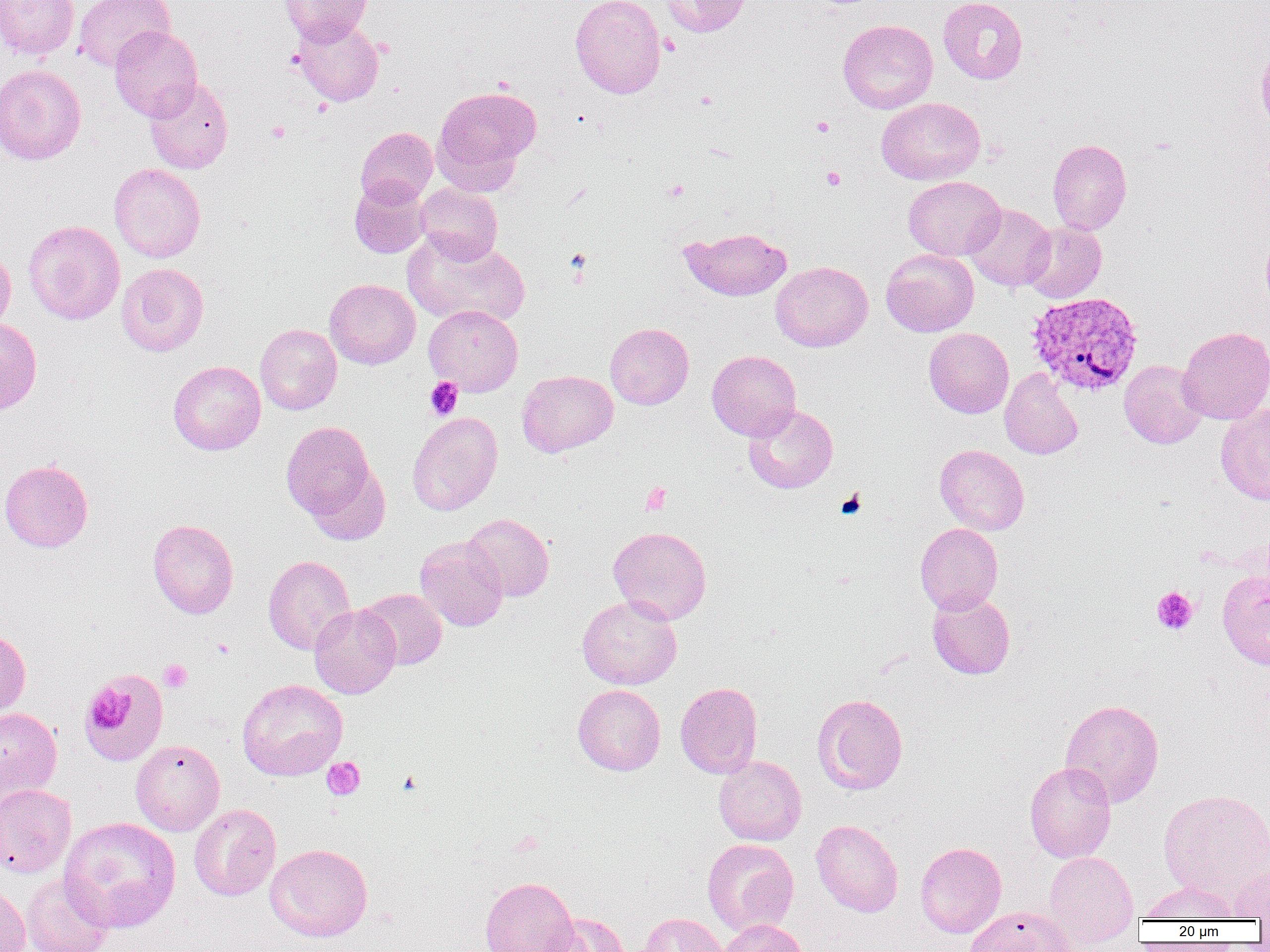
Approximate bounding boxes as named x1/y1/x2/y2 corners in pixels. Platelet locations (subset): (x1=811, y1=116, x2=834, y2=137), (x1=266, y1=121, x2=290, y2=143), (x1=821, y1=166, x2=846, y2=190), (x1=664, y1=179, x2=689, y2=201), (x1=425, y1=378, x2=463, y2=420), (x1=641, y1=482, x2=671, y2=515), (x1=836, y1=490, x2=866, y2=519), (x1=1151, y1=586, x2=1198, y2=634), (x1=158, y1=659, x2=192, y2=693), (x1=83, y1=686, x2=130, y2=733), (x1=322, y1=757, x2=365, y2=800), (x1=397, y1=771, x2=423, y2=796). Plasmodium vivax-infected red blood cell locations: (x1=1026, y1=291, x2=1144, y2=396). Uninfected red blood cell locations (subset): (x1=0, y1=0, x2=79, y2=61), (x1=73, y1=0, x2=174, y2=72), (x1=279, y1=0, x2=371, y2=45), (x1=570, y1=0, x2=666, y2=98), (x1=659, y1=0, x2=751, y2=37), (x1=939, y1=0, x2=1028, y2=84), (x1=291, y1=16, x2=384, y2=107), (x1=837, y1=19, x2=938, y2=114), (x1=109, y1=25, x2=202, y2=121), (x1=1256, y1=45, x2=1270, y2=134), (x1=0, y1=64, x2=87, y2=165), (x1=144, y1=78, x2=234, y2=174), (x1=433, y1=85, x2=540, y2=185), (x1=877, y1=97, x2=985, y2=185), (x1=355, y1=126, x2=438, y2=207), (x1=1047, y1=139, x2=1132, y2=235), (x1=109, y1=163, x2=206, y2=263), (x1=903, y1=176, x2=1005, y2=260), (x1=350, y1=179, x2=432, y2=258), (x1=416, y1=183, x2=503, y2=264), (x1=965, y1=204, x2=1055, y2=292), (x1=24, y1=220, x2=125, y2=325), (x1=1022, y1=222, x2=1107, y2=303), (x1=679, y1=227, x2=792, y2=301), (x1=1260, y1=229, x2=1270, y2=308), (x1=402, y1=232, x2=531, y2=329), (x1=0, y1=247, x2=15, y2=333), (x1=881, y1=248, x2=979, y2=337), (x1=770, y1=261, x2=873, y2=351), (x1=116, y1=262, x2=209, y2=356), (x1=324, y1=279, x2=420, y2=369), (x1=424, y1=305, x2=523, y2=396), (x1=0, y1=317, x2=42, y2=413), (x1=255, y1=323, x2=342, y2=415), (x1=605, y1=323, x2=694, y2=409), (x1=1177, y1=326, x2=1270, y2=424), (x1=924, y1=327, x2=1013, y2=418), (x1=707, y1=350, x2=801, y2=440), (x1=168, y1=360, x2=266, y2=455), (x1=1119, y1=360, x2=1207, y2=448), (x1=1000, y1=368, x2=1083, y2=459), (x1=517, y1=370, x2=618, y2=457), (x1=1216, y1=403, x2=1270, y2=505), (x1=743, y1=404, x2=838, y2=493), (x1=407, y1=412, x2=502, y2=515), (x1=281, y1=421, x2=378, y2=523), (x1=934, y1=444, x2=1029, y2=535), (x1=929, y1=445, x2=1012, y2=614), (x1=0, y1=459, x2=93, y2=552), (x1=306, y1=462, x2=390, y2=546), (x1=462, y1=513, x2=554, y2=601), (x1=147, y1=519, x2=239, y2=618), (x1=915, y1=523, x2=1003, y2=614), (x1=608, y1=525, x2=712, y2=624), (x1=414, y1=535, x2=509, y2=631), (x1=263, y1=555, x2=356, y2=655), (x1=1218, y1=570, x2=1270, y2=668), (x1=358, y1=588, x2=447, y2=669), (x1=927, y1=591, x2=1015, y2=679), (x1=577, y1=595, x2=682, y2=690), (x1=309, y1=604, x2=401, y2=699), (x1=0, y1=627, x2=30, y2=720), (x1=237, y1=678, x2=347, y2=780), (x1=675, y1=682, x2=762, y2=778), (x1=573, y1=684, x2=666, y2=775), (x1=812, y1=694, x2=908, y2=795), (x1=1060, y1=698, x2=1164, y2=808), (x1=0, y1=707, x2=62, y2=805), (x1=131, y1=740, x2=225, y2=835), (x1=713, y1=756, x2=806, y2=845), (x1=1024, y1=761, x2=1116, y2=863), (x1=0, y1=784, x2=76, y2=878), (x1=1158, y1=788, x2=1270, y2=906), (x1=189, y1=804, x2=281, y2=901), (x1=59, y1=816, x2=181, y2=933), (x1=811, y1=819, x2=903, y2=917), (x1=701, y1=838, x2=799, y2=936), (x1=915, y1=842, x2=1007, y2=937), (x1=265, y1=843, x2=373, y2=942), (x1=1043, y1=850, x2=1140, y2=946), (x1=1232, y1=859, x2=1270, y2=919), (x1=21, y1=873, x2=113, y2=952), (x1=480, y1=876, x2=579, y2=952), (x1=1140, y1=880, x2=1240, y2=922), (x1=0, y1=882, x2=30, y2=952), (x1=965, y1=906, x2=1077, y2=952), (x1=539, y1=912, x2=630, y2=952), (x1=638, y1=913, x2=727, y2=952), (x1=719, y1=919, x2=807, y2=952). Slide-level diagnosis: Plasmodium vivax. Light microscopy. Thin blood smear. Captured at 1000x magnification. Image is 1270×952 pixels. Single field of view.